State which parasite is depicted.
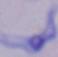

This is a trypanosome.

Micrograph. 1000x magnification.